Identify the malaria species.
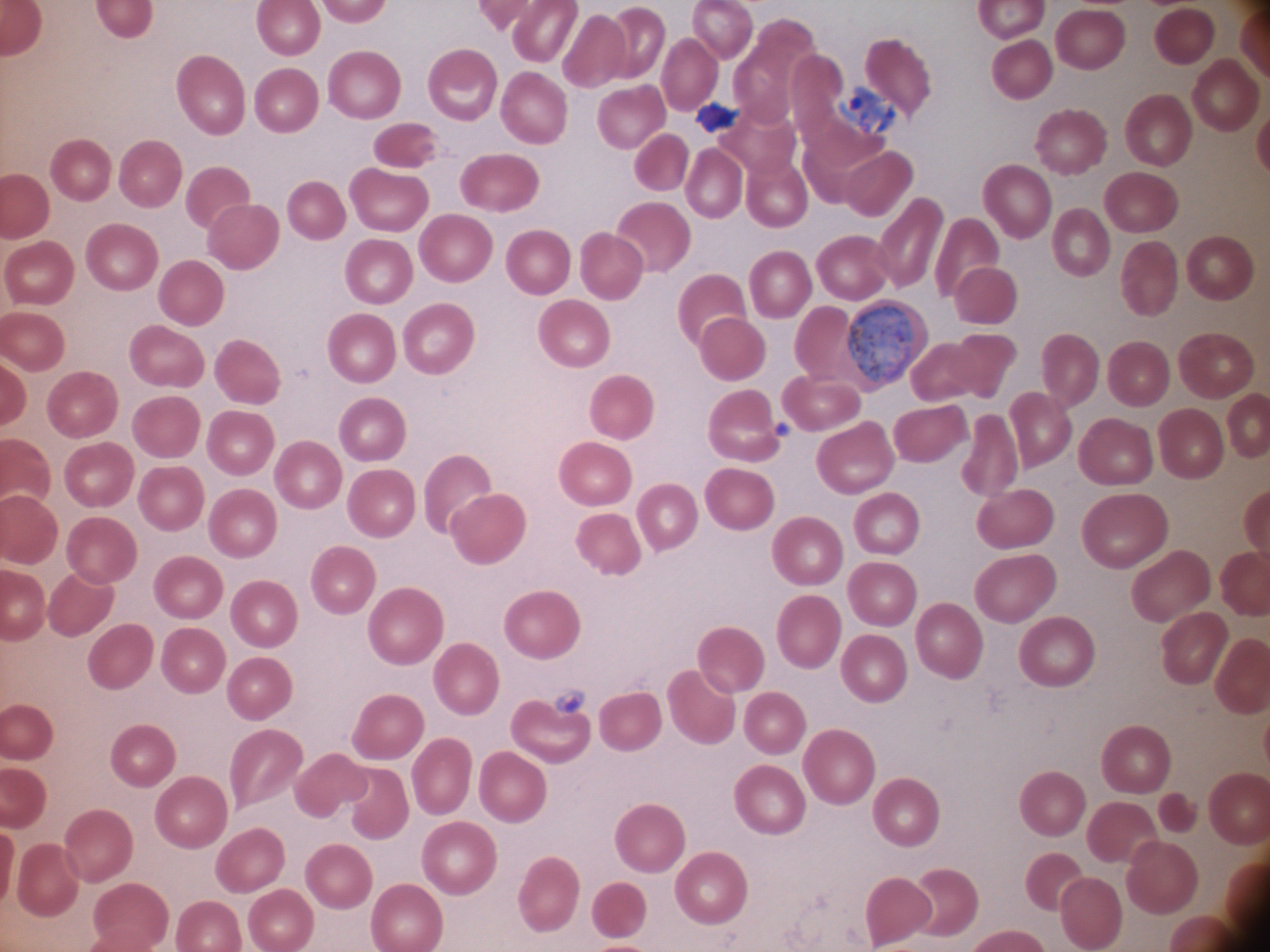
Plasmodium ovale.

Approximate bounding boxes as [x1, y1, x2, y2] in pixels, from the source annotation, which is not necessarily exhaustive. Gametocyte locations: [845, 306, 918, 383]. Single field of view. Giemsa-stained preparation. Acquired with a Leica DM2000 optical microscope and its built-in camera. Image is 1270×952 pixels. Captured at 100x magnification. Thin blood smear.